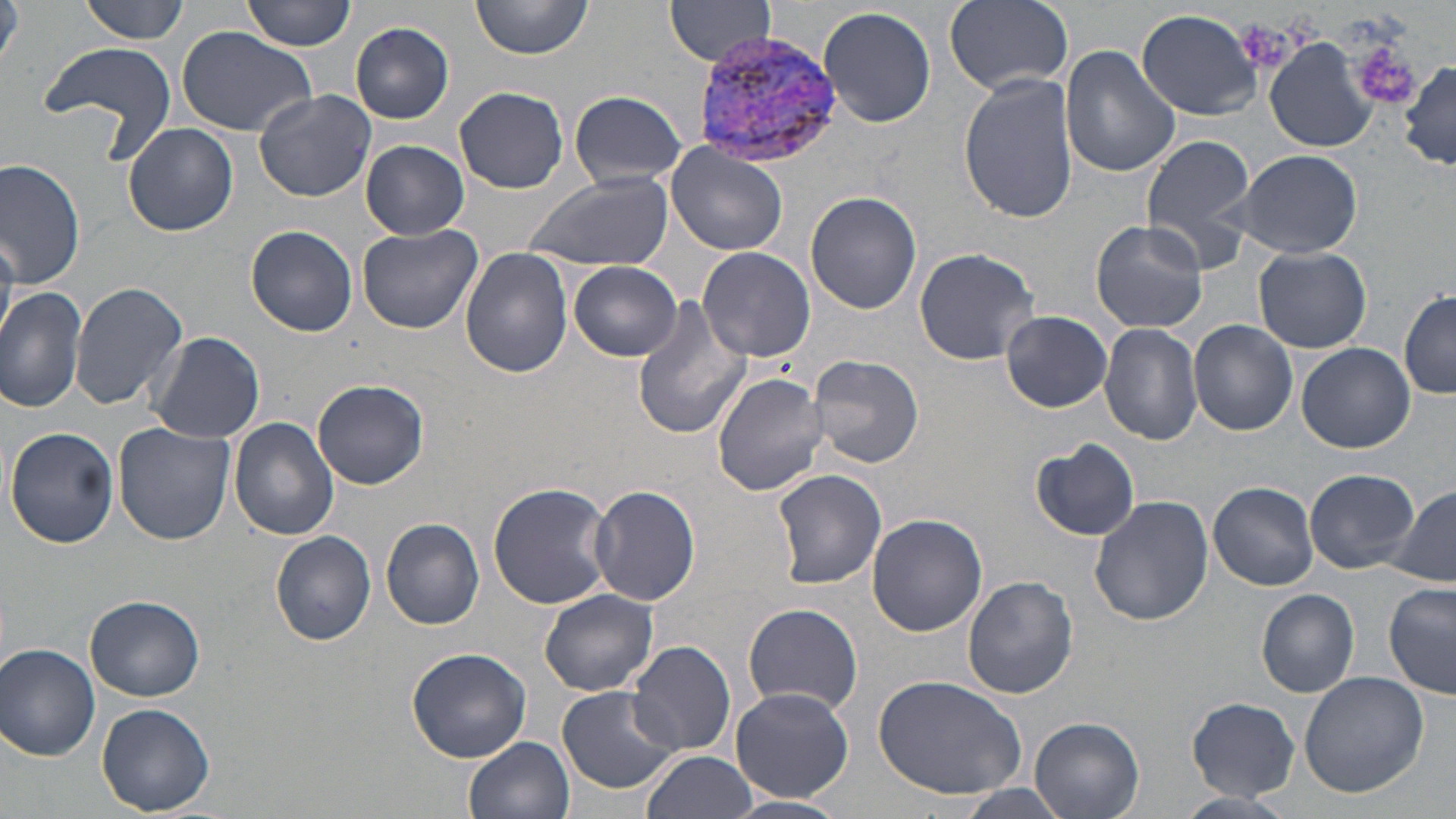

Approximate bounding boxes as (x1,y1)-(x2,y2) corner pairs in pixels. Platelet locations: (1350,39)-(1422,111). Uninfected red blood cell locations: (81,0)-(191,43), (244,0)-(358,51), (471,0)-(591,60), (667,0)-(776,65), (944,0)-(1074,93), (0,1)-(24,77), (819,6)-(937,128), (1136,9)-(1262,119), (350,21)-(455,123), (173,25)-(317,136), (37,39)-(179,162), (1267,40)-(1378,152), (1061,46)-(1180,178), (1400,60)-(1456,167), (958,72)-(1080,226), (455,86)-(569,194), (253,89)-(376,202), (569,89)-(686,192), (122,123)-(238,237), (1140,132)-(1260,271), (361,140)-(469,239), (667,144)-(787,255), (1236,148)-(1364,258), (0,159)-(84,291), (524,173)-(674,273), (806,191)-(921,315), (1091,219)-(1208,333), (359,224)-(483,334), (247,225)-(357,337), (913,246)-(1040,367), (1252,246)-(1371,353), (460,247)-(573,378), (698,247)-(815,363), (569,260)-(683,361), (71,280)-(189,411), (0,288)-(90,413), (1399,291)-(1455,401), (630,298)-(756,440), (1002,310)-(1112,413), (1188,320)-(1298,435), (1100,323)-(1203,445), (149,330)-(265,443), (1297,342)-(1415,453), (809,354)-(925,469), (712,372)-(832,497), (313,378)-(429,490), (229,417)-(338,540), (113,424)-(235,547), (6,427)-(119,548), (1032,440)-(1140,542), (771,468)-(887,590), (1305,469)-(1419,573), (1209,482)-(1319,589), (488,483)-(615,610), (588,484)-(701,606), (1387,486)-(1456,589), (1089,496)-(1213,627), (867,513)-(987,636), (382,518)-(484,629), (271,531)-(376,646), (961,574)-(1078,699), (1383,582)-(1456,698), (539,589)-(658,696), (1257,589)-(1359,697), (86,595)-(204,702), (742,603)-(862,714), (1267,634)-(1387,775), (627,641)-(735,757), (1,643)-(101,761), (406,646)-(532,763), (1298,671)-(1428,798), (872,675)-(1028,800), (556,684)-(683,795), (731,686)-(853,802), (1187,698)-(1300,799), (97,703)-(216,816), (1030,717)-(1145,819), (463,736)-(574,819), (643,750)-(758,819). Plasmodium vivax-infected red blood cell locations: (690,29)-(844,171). Slide-level diagnosis: Plasmodium vivax. May-Grünwald-Giemsa-stained preparation. Thin blood smear. 1000x magnification. Optical microscopy. Single field of view. Image is 1456×819 pixels.